Locate every blood parasite and identify its species.
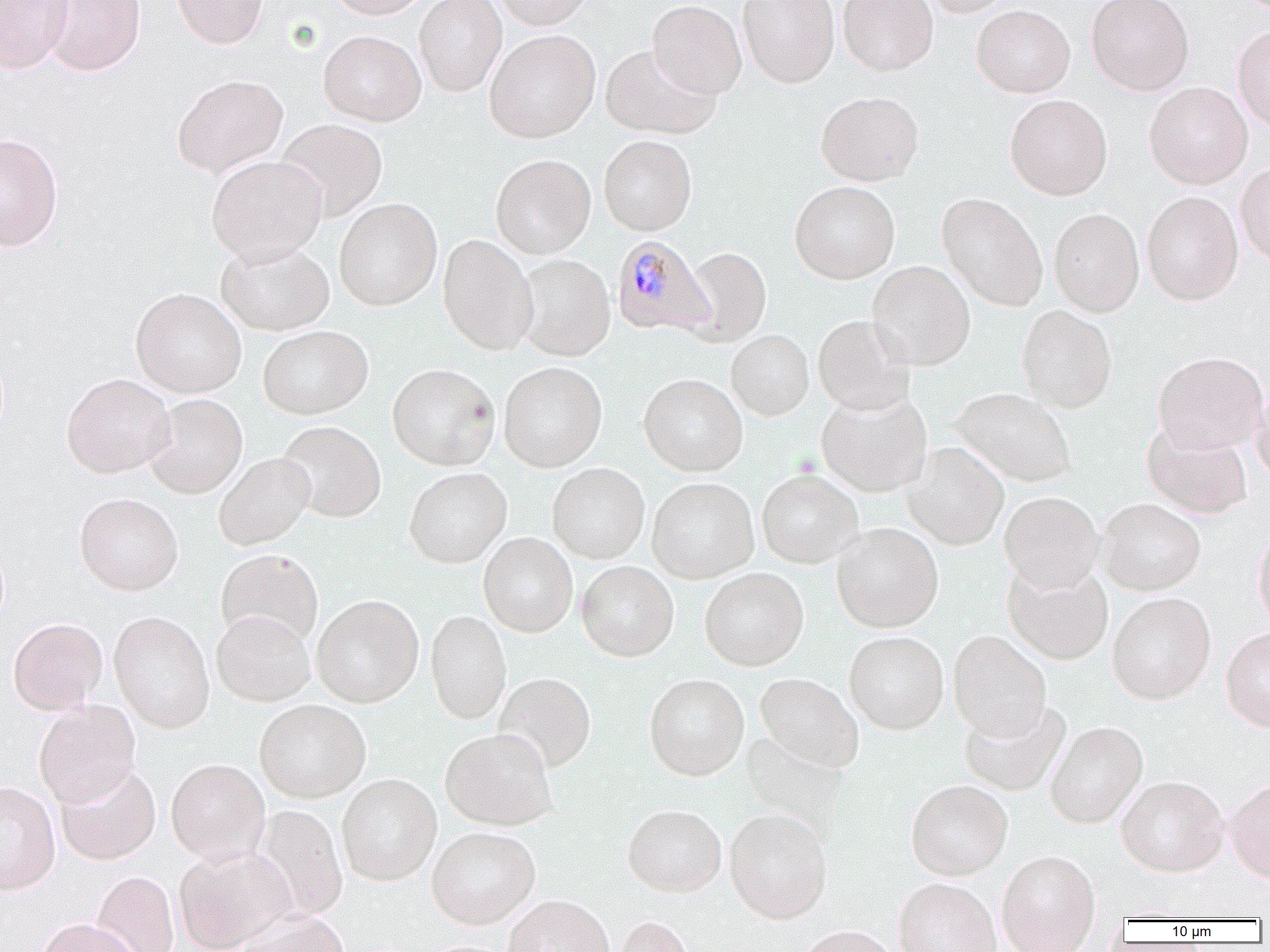
Approximate bounding boxes as named x1/y1/x2/y2 corners in pixels.
Plasmodium malariae-infected red blood cells: (x1=611, y1=235, x2=714, y2=337).
No Plasmodium falciparum, Plasmodium ovale, Plasmodium vivax, Babesia divergens, or Trypanosoma brucei observed.

slide-level diagnosis = Plasmodium malariae
image size = 1270×952 pixels
magnification = 1000x
uninfected red blood cell locations = approximate bounding boxes as named x1/y1/x2/y2 corners in pixels: (x1=0, y1=0, x2=72, y2=73), (x1=42, y1=0, x2=146, y2=77), (x1=171, y1=0, x2=268, y2=48), (x1=326, y1=0, x2=434, y2=19), (x1=413, y1=0, x2=507, y2=97), (x1=490, y1=0, x2=595, y2=30), (x1=647, y1=0, x2=747, y2=99), (x1=738, y1=0, x2=839, y2=88), (x1=838, y1=0, x2=938, y2=76), (x1=918, y1=0, x2=1016, y2=17), (x1=1086, y1=0, x2=1194, y2=95), (x1=971, y1=4, x2=1075, y2=98), (x1=1232, y1=25, x2=1270, y2=132), (x1=484, y1=29, x2=600, y2=143), (x1=318, y1=30, x2=426, y2=126), (x1=600, y1=44, x2=721, y2=140), (x1=171, y1=74, x2=288, y2=178), (x1=1144, y1=81, x2=1253, y2=189), (x1=815, y1=91, x2=924, y2=186), (x1=1005, y1=94, x2=1112, y2=201), (x1=275, y1=118, x2=388, y2=221), (x1=0, y1=133, x2=64, y2=251), (x1=598, y1=135, x2=697, y2=236), (x1=206, y1=154, x2=327, y2=265), (x1=490, y1=154, x2=596, y2=259), (x1=1235, y1=161, x2=1270, y2=266), (x1=789, y1=180, x2=900, y2=284), (x1=1141, y1=191, x2=1243, y2=305), (x1=937, y1=193, x2=1048, y2=311), (x1=334, y1=198, x2=442, y2=311), (x1=1049, y1=208, x2=1144, y2=317), (x1=437, y1=235, x2=538, y2=355), (x1=215, y1=241, x2=335, y2=336), (x1=681, y1=247, x2=772, y2=347), (x1=515, y1=254, x2=615, y2=361), (x1=867, y1=260, x2=975, y2=371), (x1=130, y1=287, x2=246, y2=398), (x1=1016, y1=305, x2=1118, y2=412), (x1=812, y1=314, x2=915, y2=416), (x1=258, y1=325, x2=373, y2=420), (x1=726, y1=330, x2=814, y2=420), (x1=1152, y1=351, x2=1268, y2=454), (x1=498, y1=361, x2=608, y2=472), (x1=387, y1=363, x2=500, y2=470), (x1=61, y1=373, x2=175, y2=478), (x1=638, y1=374, x2=748, y2=476), (x1=1250, y1=380, x2=1270, y2=485), (x1=951, y1=387, x2=1077, y2=488), (x1=816, y1=391, x2=932, y2=497), (x1=143, y1=394, x2=248, y2=499), (x1=277, y1=421, x2=386, y2=523), (x1=1142, y1=421, x2=1253, y2=519), (x1=902, y1=442, x2=1009, y2=550), (x1=213, y1=452, x2=316, y2=551), (x1=547, y1=463, x2=650, y2=563), (x1=404, y1=467, x2=512, y2=568), (x1=757, y1=469, x2=863, y2=568), (x1=647, y1=477, x2=760, y2=583), (x1=999, y1=491, x2=1104, y2=594), (x1=74, y1=492, x2=183, y2=596), (x1=1096, y1=498, x2=1206, y2=596), (x1=831, y1=523, x2=944, y2=633), (x1=1253, y1=525, x2=1270, y2=635), (x1=478, y1=532, x2=578, y2=637), (x1=215, y1=549, x2=323, y2=648), (x1=576, y1=561, x2=679, y2=662), (x1=1002, y1=561, x2=1114, y2=665), (x1=699, y1=567, x2=809, y2=671), (x1=1107, y1=593, x2=1216, y2=704), (x1=311, y1=595, x2=424, y2=707), (x1=425, y1=610, x2=511, y2=724), (x1=108, y1=611, x2=215, y2=733), (x1=211, y1=611, x2=316, y2=706), (x1=8, y1=617, x2=108, y2=714), (x1=1220, y1=627, x2=1270, y2=732), (x1=844, y1=631, x2=949, y2=734), (x1=948, y1=631, x2=1052, y2=742), (x1=494, y1=673, x2=596, y2=773), (x1=755, y1=673, x2=864, y2=773), (x1=644, y1=674, x2=749, y2=781), (x1=254, y1=700, x2=371, y2=803), (x1=958, y1=700, x2=1071, y2=797), (x1=33, y1=701, x2=141, y2=808), (x1=1045, y1=722, x2=1149, y2=829), (x1=440, y1=728, x2=558, y2=830), (x1=165, y1=759, x2=270, y2=867), (x1=55, y1=762, x2=161, y2=865), (x1=336, y1=774, x2=442, y2=886), (x1=1115, y1=777, x2=1229, y2=877), (x1=1226, y1=778, x2=1270, y2=884), (x1=906, y1=780, x2=1013, y2=880), (x1=0, y1=781, x2=61, y2=895), (x1=252, y1=805, x2=348, y2=921), (x1=622, y1=805, x2=727, y2=898), (x1=725, y1=808, x2=832, y2=923), (x1=427, y1=827, x2=541, y2=929), (x1=175, y1=845, x2=298, y2=951), (x1=997, y1=850, x2=1101, y2=952), (x1=91, y1=871, x2=179, y2=952), (x1=893, y1=878, x2=1001, y2=952), (x1=503, y1=895, x2=614, y2=952), (x1=231, y1=910, x2=350, y2=952), (x1=613, y1=915, x2=694, y2=952), (x1=35, y1=918, x2=143, y2=952), (x1=794, y1=925, x2=899, y2=952)
modality = optical microscopy
preparation = thin blood smear
field of view = single